State which parasite is depicted.
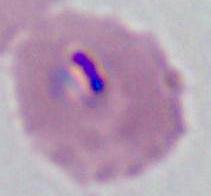

This is Plasmodium.

Summary:
  - Magnification: 400x or 1000x
  - Modality: photomicrograph